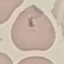

Malaria status: uninfected. Giemsa stain. Cell patch, automatically extracted from a larger field of view and resized to 64 × 64 pixels. Thin blood film. Acquired by smartphone through the microscope eyepiece.